Assess this cell for malaria.
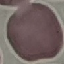
Uninfected.

capture: smartphone camera at the microscope eyepiece
preparation: thin blood smear
stain: Giemsa
image_type: cell patch, automatically extracted from a larger field of view and resized to 64 × 64 pixels